Assess the morphology of the erythrocytes.
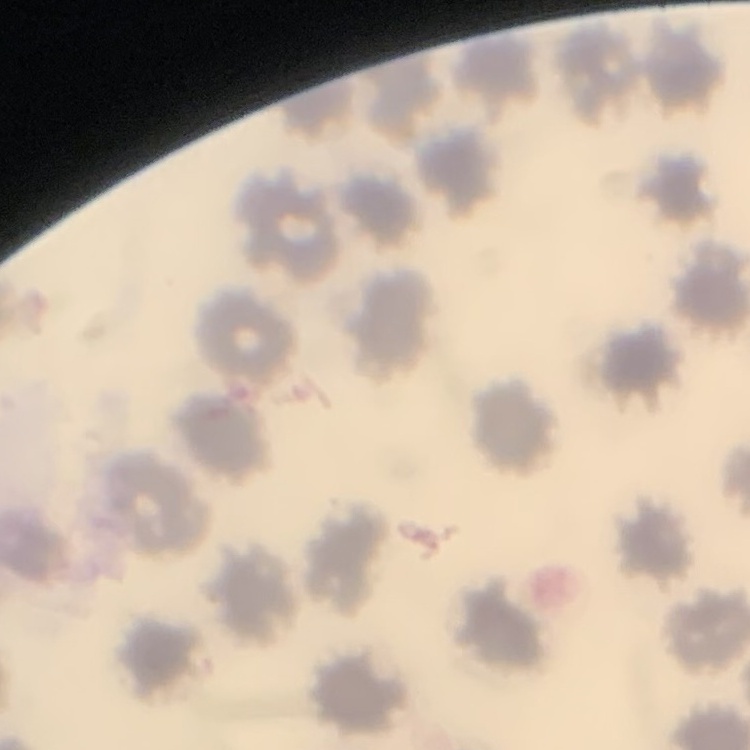
No rouleaux formation.

Summary:
  - Preparation: thin blood smear
  - Image type: one tile cut from a larger photomicrograph
  - Stain: Field's or Giemsa